Name the blood parasite species.
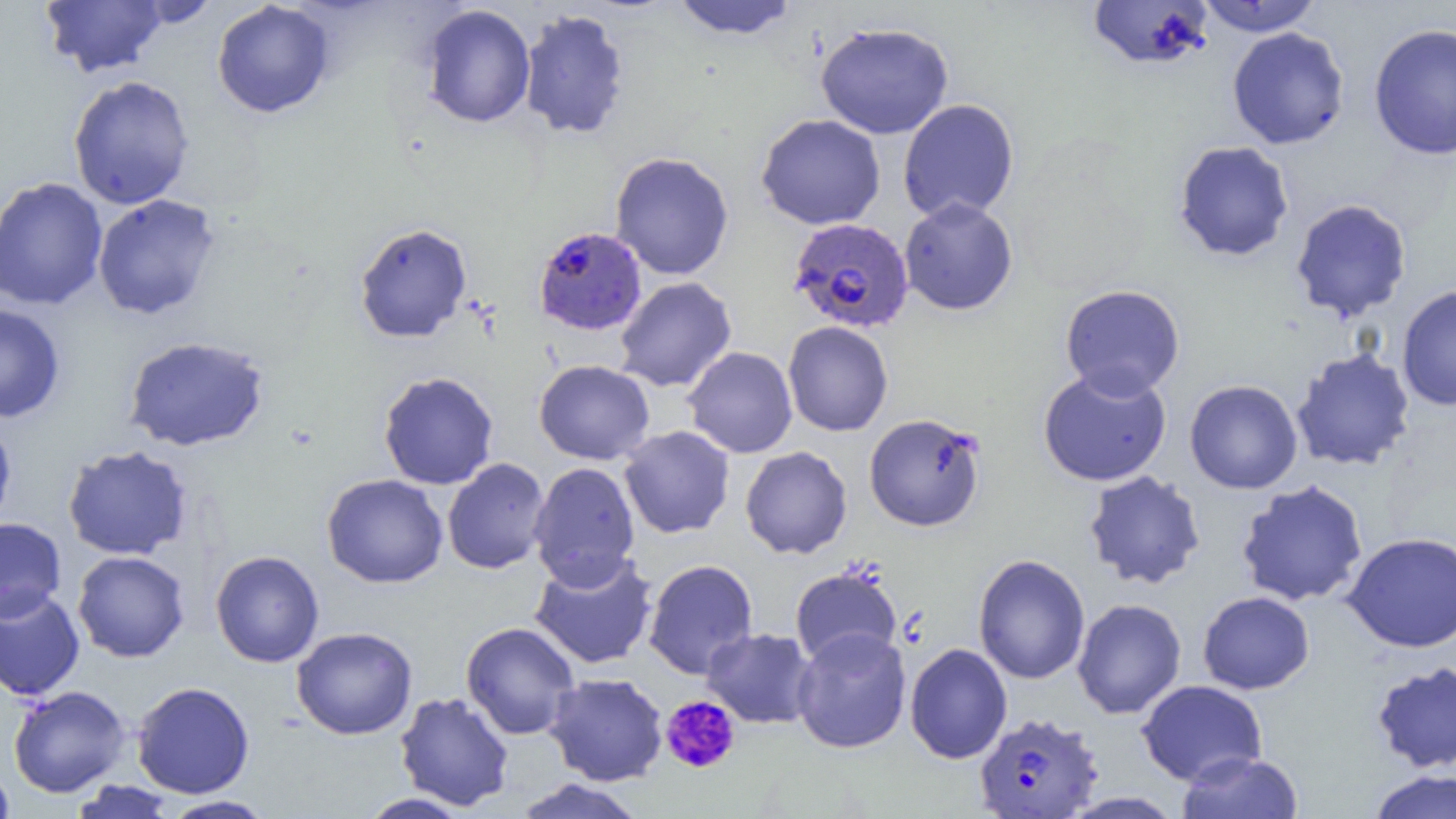

Plasmodium falciparum.

Summary:
  - Coordinate format: approximate bounding boxes as [x1, y1, x2, y2] in pixels
  - Plasmodium falciparum-infected red blood cell locations (subset): [788, 217, 915, 333], [533, 226, 647, 336], [973, 711, 1103, 817]
  - Uninfected red blood cell locations (subset): [40, 0, 168, 78], [670, 0, 799, 40], [1086, 0, 1215, 71], [1195, 0, 1324, 36], [131, 1, 221, 28], [211, 1, 335, 118], [420, 4, 537, 129], [517, 8, 630, 141], [815, 21, 954, 139], [1367, 22, 1456, 160], [1227, 26, 1350, 150], [67, 75, 196, 210], [897, 98, 1019, 223], [1173, 140, 1295, 262], [609, 151, 734, 280], [0, 177, 108, 311], [92, 194, 221, 321], [899, 198, 1017, 316], [1289, 198, 1413, 323], [354, 222, 473, 343], [614, 276, 737, 393], [1059, 284, 1186, 400], [1396, 284, 1456, 411], [0, 303, 65, 423], [783, 321, 894, 437], [123, 336, 270, 452], [683, 346, 798, 458], [1290, 348, 1416, 472], [533, 359, 655, 465], [1037, 367, 1173, 487], [378, 371, 499, 490], [1184, 379, 1303, 494], [864, 412, 986, 532], [0, 416, 17, 530], [619, 426, 735, 539], [62, 445, 193, 560], [740, 446, 852, 559], [442, 458, 551, 574], [528, 462, 641, 588], [1083, 470, 1206, 590], [321, 473, 448, 589], [1235, 479, 1369, 607], [0, 517, 66, 621], [1342, 531, 1456, 652], [210, 550, 325, 667], [72, 551, 190, 662], [528, 552, 659, 670], [972, 554, 1090, 685], [643, 559, 759, 680], [790, 565, 903, 668], [0, 585, 85, 701], [1197, 590, 1315, 694], [1072, 598, 1187, 719], [460, 621, 581, 740], [291, 626, 418, 739], [701, 628, 818, 729], [792, 628, 911, 754], [905, 643, 1012, 764], [1371, 661, 1456, 773], [544, 673, 668, 786], [1136, 680, 1267, 786], [131, 681, 255, 798], [8, 685, 132, 798], [394, 691, 515, 811], [1176, 751, 1303, 819], [0, 763, 16, 819], [1366, 769, 1456, 819], [513, 778, 647, 819], [67, 780, 180, 819], [1060, 791, 1185, 818], [357, 793, 473, 818], [160, 795, 276, 818]
  - Platelet locations: [660, 694, 741, 774]
  - Modality: light microscopy
  - Image size: 1456×819 pixels
  - Magnification: 1000x
  - Field of view: single
  - Preparation: thin blood smear